Report the malaria status of this cell.
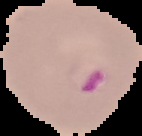

Parasitized.

image_size: 142×136 pixels
preparation: thin blood smear
image_type: cell region segmented out of the field of view; surrounding area masked to black